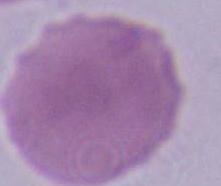

Summary:
  - Identification: erythrocyte
  - Magnification: 1000x
  - Modality: micrograph